Report the malaria status of this cell.
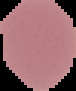
It is uninfected.

Summary:
  - Preparation: thin blood film
  - Image type: cell region segmented out of the field of view; surrounding area masked to black
  - Image size: 76×91 pixels